Identify the blood parasite species.
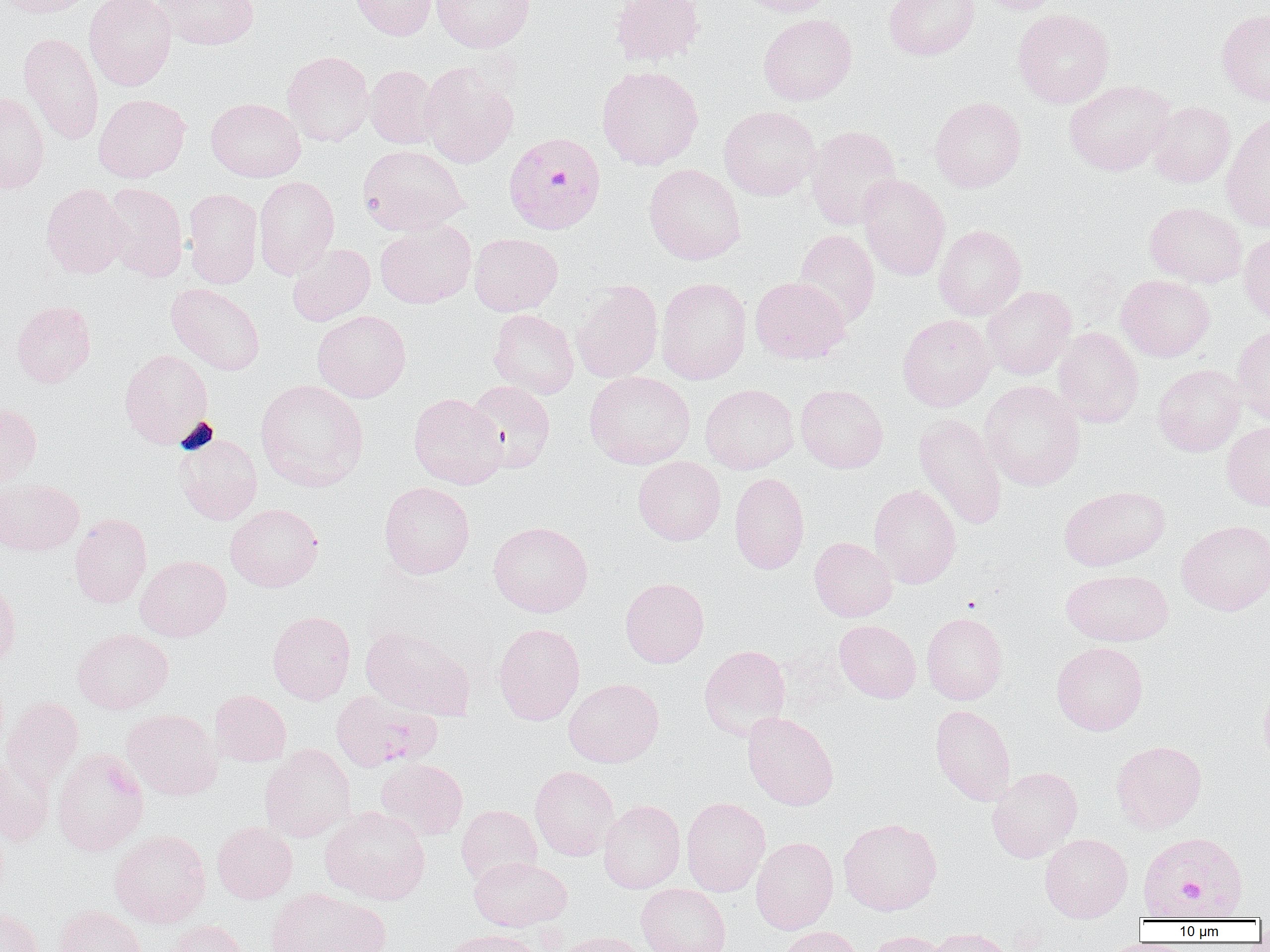

Plasmodium falciparum.

Summary:
  - Coordinate format: approximate bounding boxes as (x1, y1, x2, y2) in pixels
  - Plasmodium falciparum-infected red blood cell locations: (506, 130, 608, 233), (331, 690, 441, 771), (1150, 819, 1245, 909)
  - Uninfected red blood cell locations: (1, 0, 97, 18), (84, 0, 176, 91), (156, 0, 260, 50), (351, 0, 436, 40), (431, 0, 535, 52), (610, 0, 705, 66), (734, 0, 836, 17), (884, 0, 980, 60), (975, 0, 1067, 14), (1013, 8, 1114, 108), (1216, 9, 1270, 108), (758, 14, 857, 105), (19, 32, 103, 145), (282, 51, 375, 146), (419, 62, 519, 169), (365, 65, 441, 149), (597, 66, 703, 170), (1064, 80, 1175, 176), (0, 91, 49, 193), (93, 94, 190, 182), (929, 96, 1026, 192), (206, 98, 306, 182), (1149, 101, 1235, 187), (719, 106, 820, 200), (1221, 111, 1270, 232), (805, 125, 902, 230), (358, 144, 469, 234), (644, 163, 746, 265), (857, 174, 950, 281), (253, 176, 339, 279), (101, 182, 188, 282), (41, 183, 129, 279), (183, 188, 263, 288), (1144, 201, 1248, 288), (375, 220, 476, 309), (934, 224, 1026, 320), (794, 229, 880, 328), (1239, 229, 1270, 323), (469, 233, 563, 316), (287, 243, 375, 326), (1116, 274, 1215, 362), (656, 277, 752, 384), (750, 277, 850, 364), (572, 280, 664, 383), (166, 283, 265, 375), (982, 285, 1077, 379), (10, 300, 96, 387), (488, 309, 579, 399), (312, 310, 411, 402), (897, 314, 996, 411), (1232, 324, 1270, 425), (1053, 327, 1144, 427), (119, 349, 214, 448), (1153, 364, 1245, 456), (584, 371, 695, 469), (255, 379, 369, 492), (465, 380, 555, 472), (979, 380, 1085, 491), (700, 383, 799, 474), (795, 385, 888, 473), (408, 392, 507, 490), (0, 402, 42, 486), (914, 412, 1008, 530), (1221, 421, 1270, 511), (175, 434, 262, 525), (633, 456, 726, 545), (729, 472, 810, 574), (0, 478, 84, 555), (379, 482, 475, 579), (869, 484, 962, 588), (1058, 484, 1170, 571), (225, 503, 324, 592), (69, 513, 152, 608), (1177, 519, 1270, 616), (488, 521, 593, 617), (809, 537, 897, 621), (135, 555, 231, 641), (1061, 568, 1174, 646), (620, 577, 709, 668), (0, 579, 21, 669), (267, 610, 356, 704), (921, 611, 1008, 705), (834, 619, 921, 703), (493, 622, 585, 725), (360, 625, 475, 720), (72, 628, 173, 714), (1051, 641, 1148, 735), (699, 644, 791, 741), (563, 678, 664, 768), (1258, 681, 1270, 770), (210, 689, 292, 766), (1, 696, 84, 790), (930, 704, 1016, 806), (122, 708, 222, 800), (742, 711, 839, 810), (1111, 739, 1206, 834), (259, 745, 355, 842), (52, 748, 148, 855), (0, 755, 54, 845), (376, 758, 467, 839), (529, 765, 620, 860), (987, 767, 1082, 863), (681, 796, 770, 896), (598, 800, 685, 893), (456, 805, 542, 887), (320, 806, 431, 905), (838, 817, 943, 916), (212, 821, 297, 903), (110, 829, 211, 927), (1040, 833, 1132, 922), (751, 837, 838, 934), (469, 856, 571, 931), (636, 883, 731, 952), (265, 887, 385, 952), (54, 905, 147, 952), (0, 906, 45, 952), (161, 920, 250, 952), (777, 925, 864, 952), (923, 927, 1015, 952), (439, 929, 543, 952), (867, 930, 951, 952), (555, 931, 647, 952)
  - Magnification: 1000x
  - Image size: 1270×952 pixels
  - Modality: optical microscopy
  - Preparation: thin blood smear
  - Field of view: single